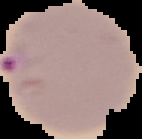

image_type: segmented cell region with the area outside set to black
result: Plasmodium parasites identified
preparation: thin blood smear
image_size: 142×139 pixels